Locate every Plasmodium parasite.
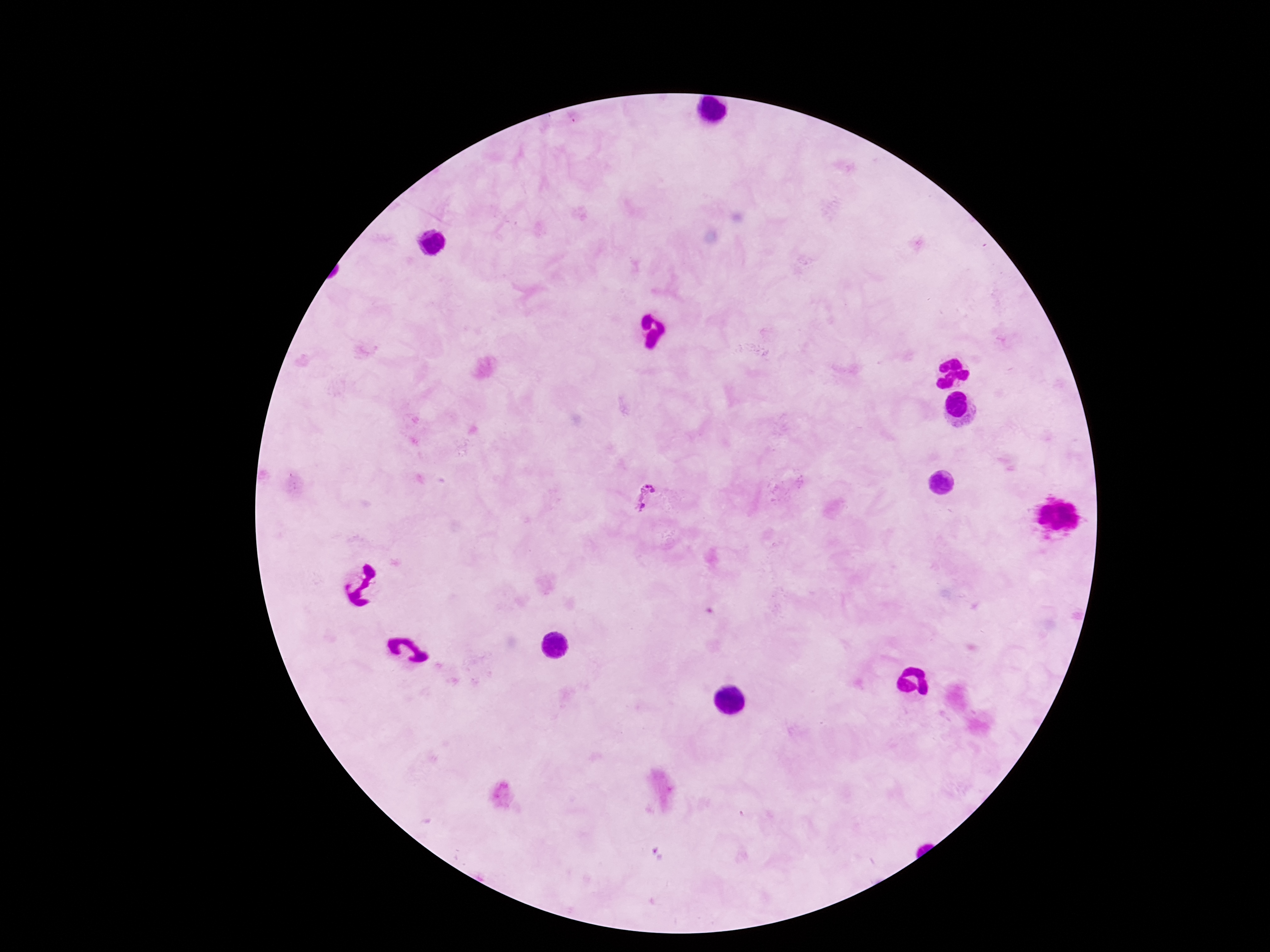

Approximate centers as [x, y] in pixels.
Plasmodium parasites: [647, 497].

Summary:
  - Magnification: 100x
  - Image size: 1270×952 pixels
  - Preparation: thick blood smear
  - Stain: Giemsa
  - Capture: smartphone camera through the microscope eyepiece
  - Patient malaria status: positive
  - Field of view: one from this slide